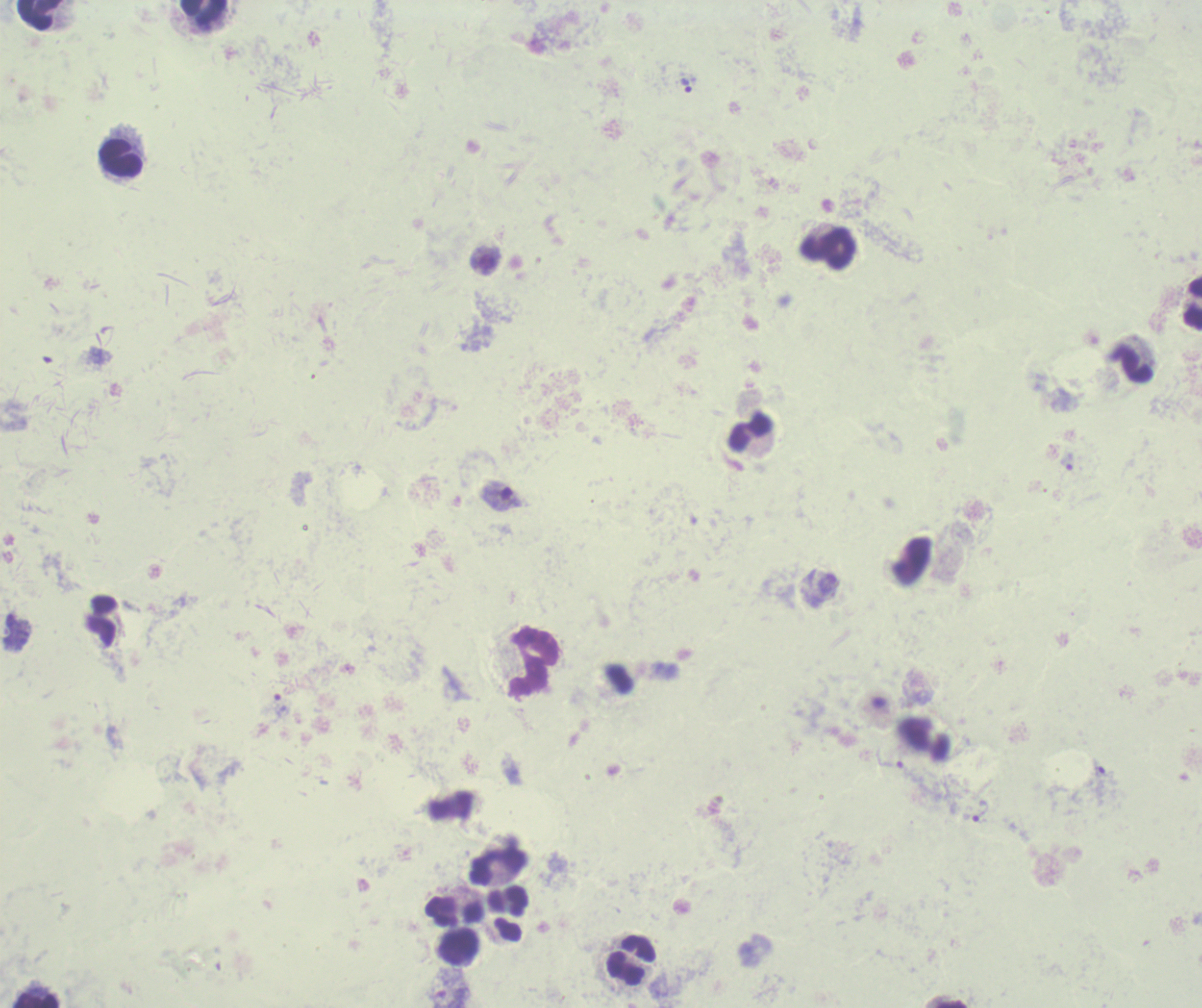
{
  "life_cycle_stages_observed": "trophozoite, gametocyte",
  "magnification": "100x",
  "result": "positive for malaria parasites",
  "image_size": "1202×1008 pixels",
  "background_quality": "poor",
  "trophozoite_locations": "approximate object centers, in pixels from the top-left corner: (x=685, y=84), (x=1068, y=462), (x=891, y=758), (x=1105, y=771), (x=980, y=811)",
  "stain": "Romanowsky",
  "gametocyte_locations": "approximate object centers, in pixels from the top-left corner: (x=501, y=495), (x=827, y=587)",
  "leukocyte_locations": "approximate object centers, in pixels from the top-left corner: (x=204, y=13), (x=39, y=14), (x=121, y=157), (x=828, y=250), (x=1192, y=303), (x=1131, y=363), (x=750, y=433), (x=533, y=661), (x=499, y=867), (x=508, y=900), (x=454, y=910), (x=458, y=947), (x=629, y=959), (x=36, y=1000)",
  "context": "previously used in an actual diagnosis",
  "field_of_view": "single",
  "preparation": "thick blood smear"
}